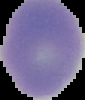
The area outside the segmented cell region is set to black. From a thin blood film. Image is 85×100 pixels. Result: negative for Plasmodium parasites.